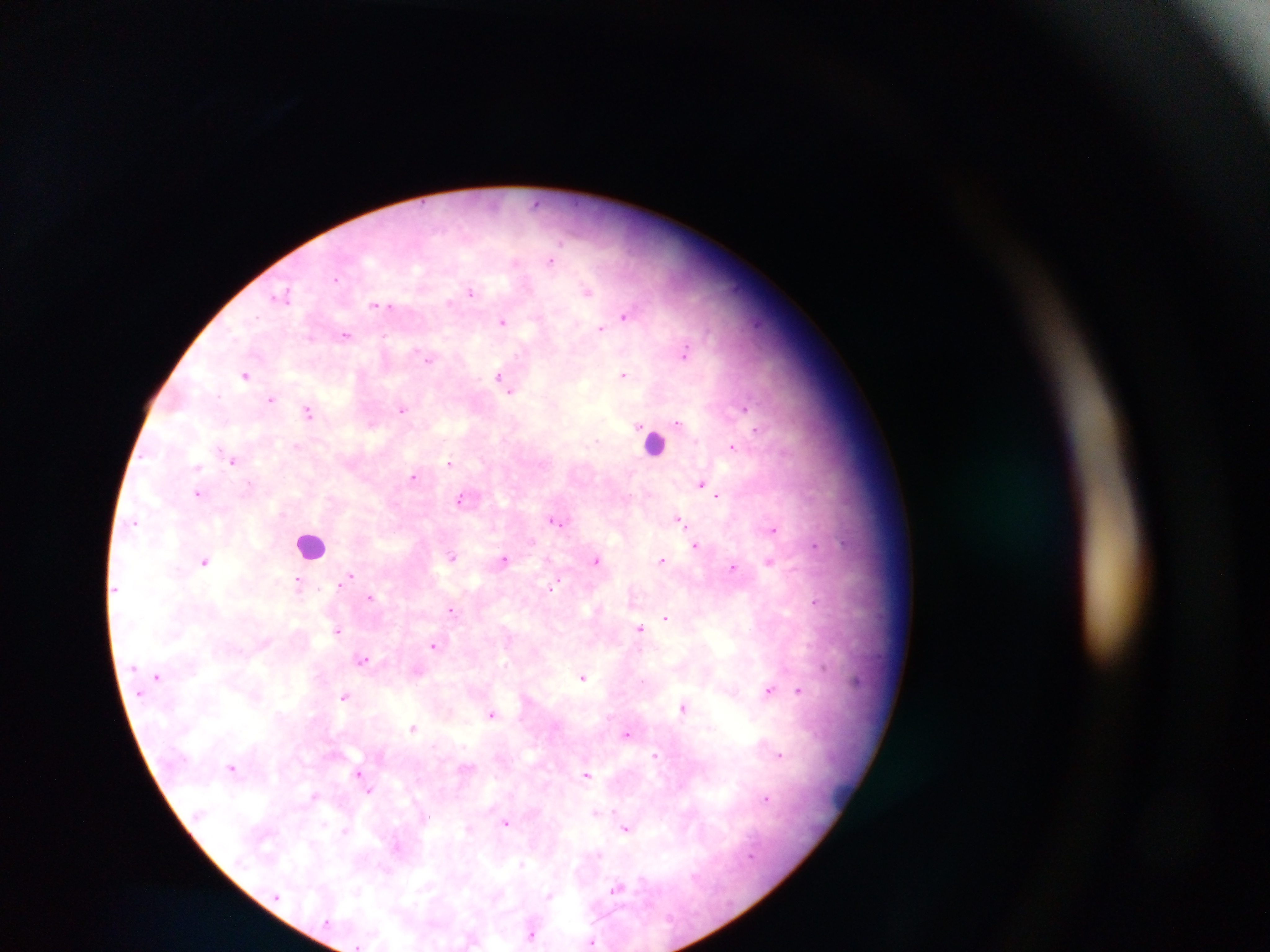
Approximate centers as (x, y) in pixels.
Summary:
  - Plasmodium parasite locations: (535, 203), (550, 261), (515, 262), (335, 278), (529, 288), (588, 290), (472, 293), (450, 301), (375, 305), (383, 305), (623, 315), (501, 321), (601, 327), (344, 336), (428, 357), (624, 374), (245, 375), (497, 375), (512, 391), (272, 399), (744, 406), (403, 409), (309, 412), (679, 423), (755, 431), (218, 445), (733, 447), (449, 462), (233, 463), (415, 477), (702, 483), (250, 484), (198, 494), (458, 500), (679, 518), (558, 520), (135, 523), (774, 529), (695, 545), (814, 545), (452, 556), (504, 559), (597, 560), (662, 560), (770, 560), (205, 562), (734, 566), (345, 580), (557, 582), (299, 583), (339, 583), (369, 597), (815, 600), (452, 610), (664, 619), (639, 628), (337, 630), (434, 646), (363, 660), (823, 667), (582, 677), (768, 690), (799, 690), (344, 696), (682, 708), (276, 712), (490, 715), (414, 726), (628, 733), (777, 752), (781, 754), (655, 755), (232, 766), (358, 771), (588, 773), (369, 790), (313, 796), (767, 799), (596, 813), (427, 817), (505, 822), (322, 826), (625, 830), (344, 831), (751, 854), (520, 863), (616, 888), (549, 894), (532, 934), (592, 940), (358, 944)
  - Field of view: single
  - Country: Ghana
  - Image size: 1270×952 pixels
  - Capture: mobile-phone photograph through a microscope
  - Preparation: thick blood film